Identify the cell.
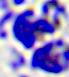
This is a leukocyte.

Summary:
  - Magnification: 400x
  - Modality: photomicrograph